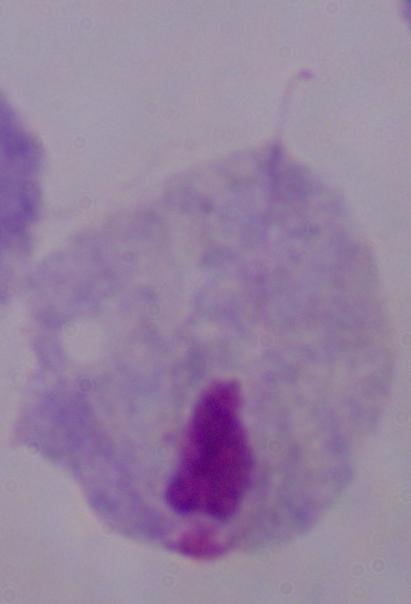
magnification = 1000x
identification = trichomonad
modality = micrograph